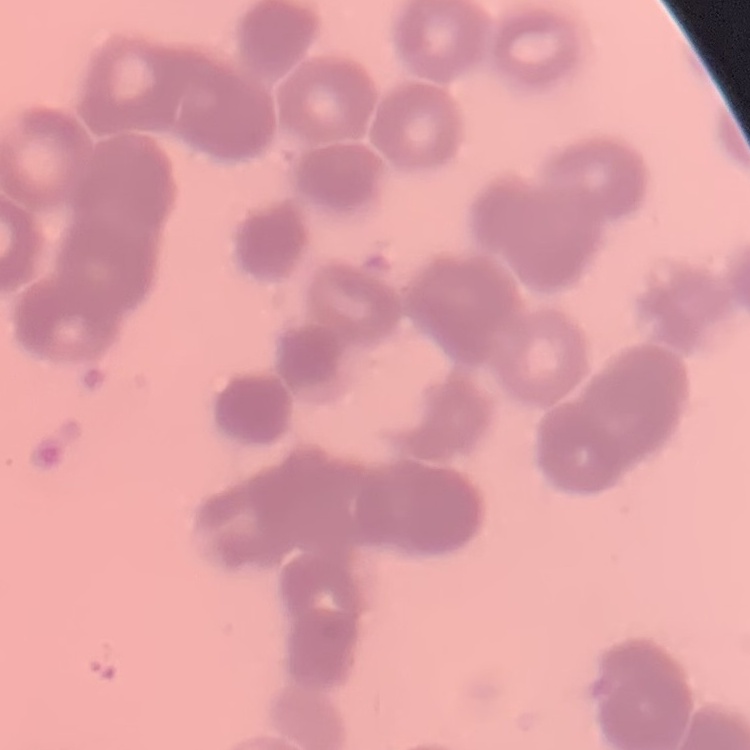

Summary:
  - Erythrocyte morphology: rouleaux formation
  - Image type: square crop of a larger photomicrograph
  - Preparation: thin peripheral smear
  - Stain: Field's or Giemsa